Locate every blood parasite and identify its species.
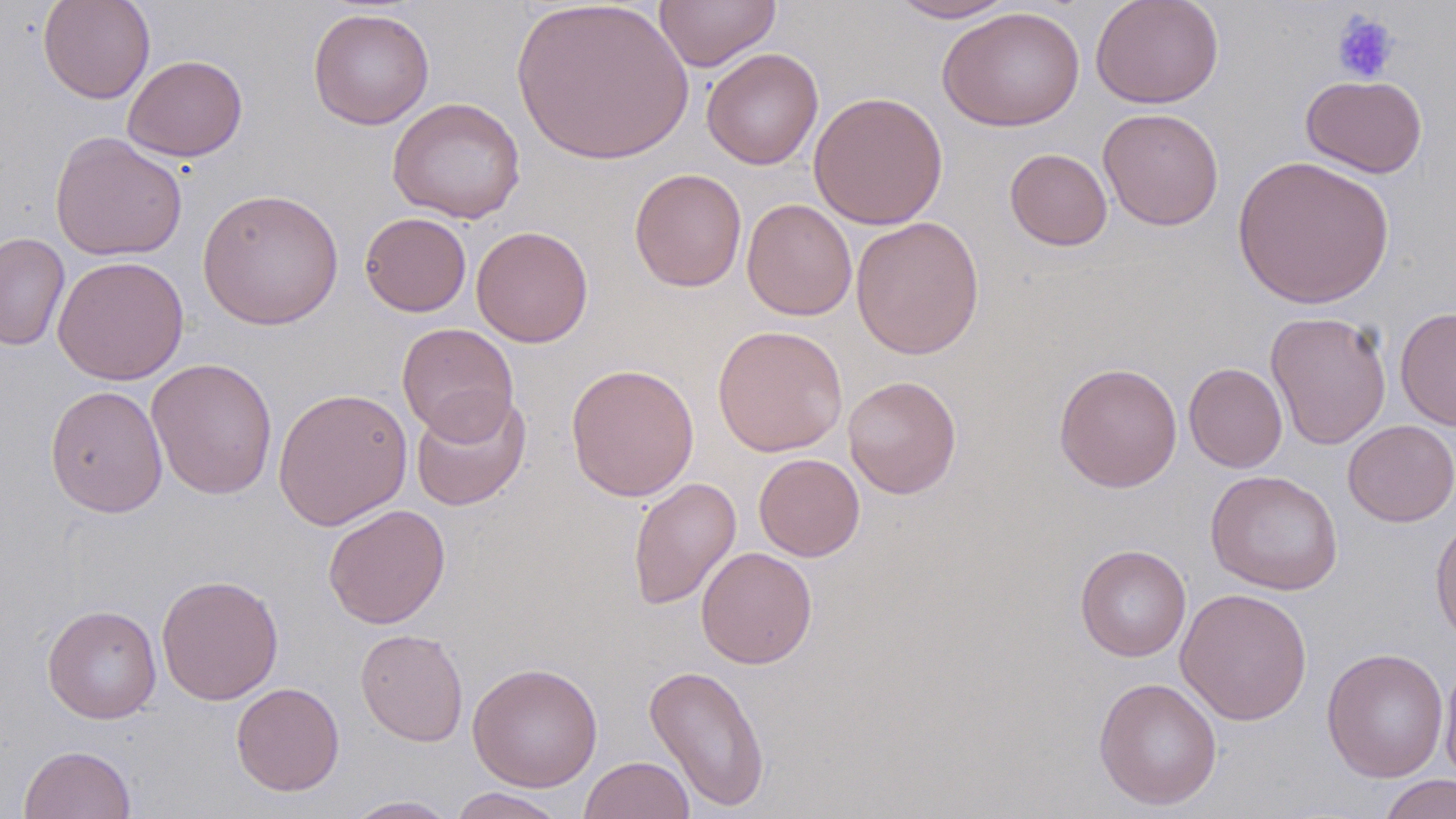
No blood parasites seen.

slide-level diagnosis = no evidence of blood parasites
preparation = thin blood smear
modality = light microscopy
field of view = one of a larger specimen
magnification = 1000x
image size = 1456×819 pixels
uninfected red blood cell locations = approximate bounding boxes as [x1, y1, x2, y2] in pixels: [38, 0, 155, 104], [510, 0, 694, 165], [886, 0, 1020, 23], [1090, 0, 1224, 109], [654, 1, 780, 71], [937, 6, 1085, 131], [308, 7, 435, 130], [701, 48, 824, 169], [123, 54, 248, 161], [1301, 74, 1428, 178], [808, 90, 948, 230], [388, 97, 526, 223], [1097, 107, 1225, 231], [49, 131, 188, 261], [1005, 148, 1113, 251], [1232, 155, 1395, 309], [628, 168, 747, 291], [197, 187, 345, 330], [742, 198, 857, 321], [360, 212, 472, 317], [851, 216, 984, 359], [471, 225, 594, 347], [0, 231, 71, 352], [52, 255, 189, 385], [1395, 306, 1456, 430], [1265, 310, 1392, 450], [397, 322, 519, 442], [712, 324, 848, 457], [146, 357, 278, 500], [1054, 362, 1182, 492], [1183, 362, 1288, 473], [566, 363, 700, 501], [842, 376, 962, 498], [44, 385, 168, 516], [273, 386, 413, 531], [410, 392, 531, 511], [1342, 420, 1456, 527], [753, 453, 865, 562], [1205, 470, 1343, 595], [627, 477, 742, 611], [323, 503, 450, 629], [1430, 516, 1456, 649], [1075, 544, 1192, 661], [696, 547, 817, 669], [155, 573, 284, 706], [1175, 587, 1312, 727], [42, 604, 162, 723], [355, 628, 469, 747], [1321, 647, 1449, 782], [1438, 656, 1456, 786], [468, 662, 603, 792], [643, 664, 771, 812], [1093, 676, 1223, 810], [231, 682, 345, 796], [19, 744, 137, 819], [578, 755, 695, 819], [1379, 774, 1456, 819], [449, 787, 569, 819], [342, 795, 461, 818]
stain = May-Grünwald-Giemsa
platelet locations = approximate bounding boxes as [x1, y1, x2, y2] in pixels: [1331, 12, 1400, 84]